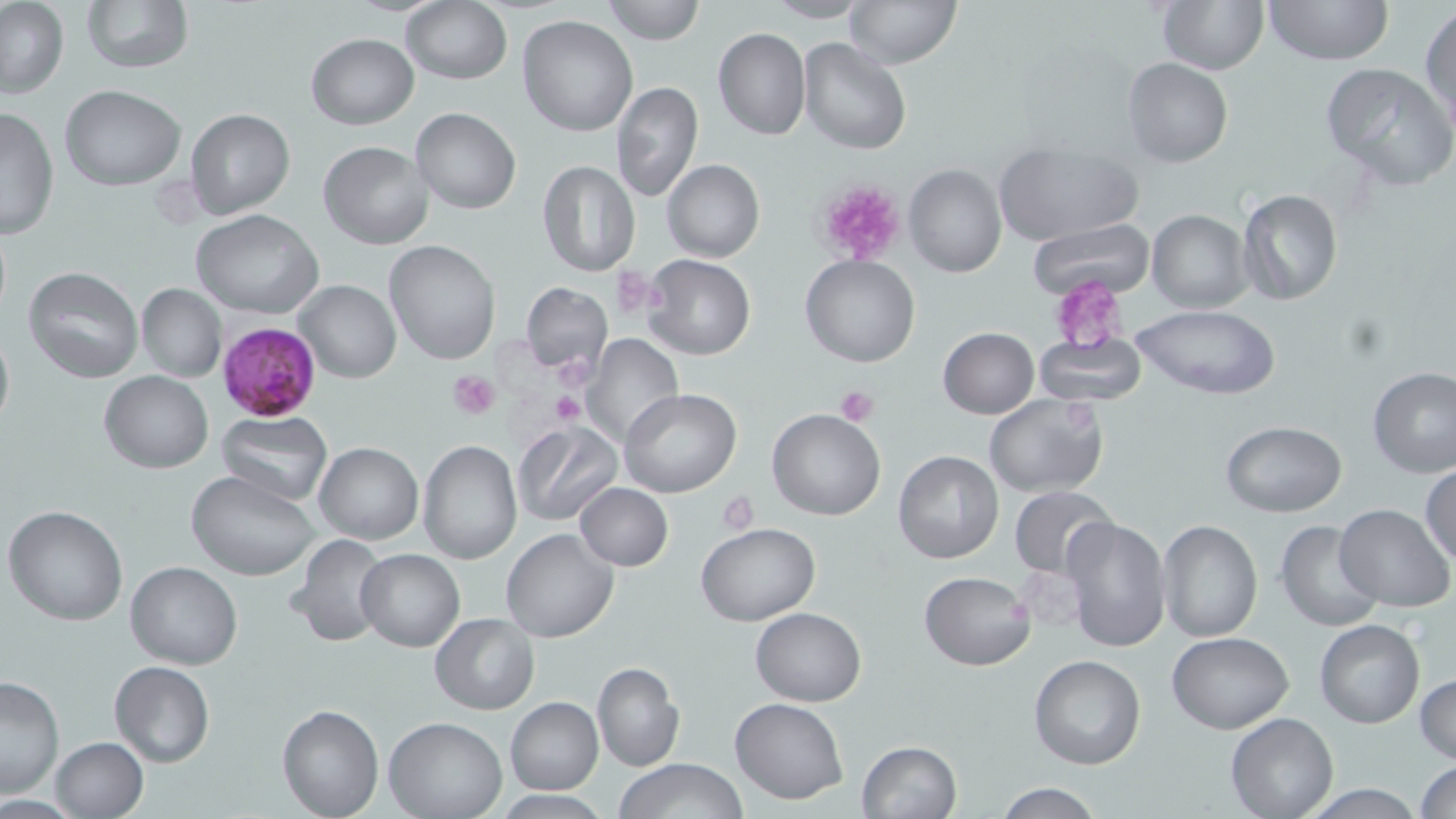
Approximate bounding boxes as (x1,y1)-(x2,y2) corner pairs in pixels. Platelet locations: (815,178)-(907,265), (611,265)-(672,323), (1051,277)-(1131,351), (555,358)-(597,390), (448,370)-(500,418), (835,386)-(879,427), (549,390)-(585,427), (716,491)-(760,537). Uninfected red blood cell locations: (1,0)-(69,100), (79,0)-(193,75), (602,0)-(704,45), (843,0)-(962,68), (1160,0)-(1267,74), (1265,0)-(1390,65), (400,2)-(511,85), (763,2)-(872,23), (1420,5)-(1455,135), (516,14)-(638,137), (713,28)-(810,141), (305,33)-(418,128), (798,37)-(911,156), (1122,57)-(1232,167), (1320,61)-(1455,192), (611,82)-(703,203), (60,85)-(186,190), (0,106)-(58,241), (410,107)-(521,214), (185,108)-(296,222), (318,140)-(434,250), (994,140)-(1142,245), (662,159)-(764,262), (536,160)-(640,276), (904,164)-(1006,278), (1237,189)-(1343,306), (193,209)-(323,319), (1146,209)-(1252,311), (1027,218)-(1154,301), (384,240)-(501,366), (641,254)-(756,361), (799,254)-(922,368), (24,267)-(144,383), (296,280)-(402,384), (522,281)-(613,378), (136,282)-(225,383), (1129,304)-(1281,400), (0,323)-(13,435), (938,327)-(1039,418), (580,333)-(685,447), (1033,335)-(1147,403), (1368,366)-(1456,478), (99,370)-(214,473), (619,387)-(742,496), (983,392)-(1109,496), (767,408)-(887,521), (216,411)-(334,507), (1220,421)-(1347,517), (513,422)-(624,527), (417,440)-(521,564), (314,442)-(422,544), (894,450)-(1003,564), (1420,465)-(1456,566), (187,469)-(321,582), (574,482)-(673,571), (1008,485)-(1116,580), (4,505)-(129,626), (1335,505)-(1453,612), (1059,515)-(1172,653), (1274,519)-(1385,633), (1158,520)-(1262,643), (697,523)-(821,625), (500,529)-(618,643), (286,535)-(388,648), (356,548)-(465,651), (125,561)-(242,669), (918,570)-(1036,671), (751,607)-(866,706), (430,613)-(540,714), (1314,619)-(1426,729), (1166,632)-(1294,734), (1028,655)-(1145,771), (591,661)-(684,772), (108,662)-(215,767), (1414,672)-(1456,765), (0,675)-(65,797), (504,696)-(603,795), (730,697)-(850,803), (277,703)-(384,817), (1225,711)-(1338,818), (383,715)-(507,818), (48,736)-(148,819), (856,740)-(961,819), (615,759)-(749,818), (1414,761)-(1456,817), (990,781)-(1107,819), (1295,784)-(1432,818). Plasmodium falciparum-infected red blood cell locations: (217,320)-(320,421). Slide-level diagnosis: Plasmodium falciparum. Thin blood smear. 1000x magnification. Optical microscopy. One field of a larger specimen. Image is 1456×819 pixels. May-Grünwald-Giemsa-stained preparation.